Assess this cell for malaria.
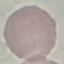

It is uninfected.

capture = smartphone through the microscope eyepiece
preparation = thin blood film
stain = Giemsa
image type = cell patch, automatically extracted from a larger field of view and resized to 64 × 64 pixels